Name the parasite shown.
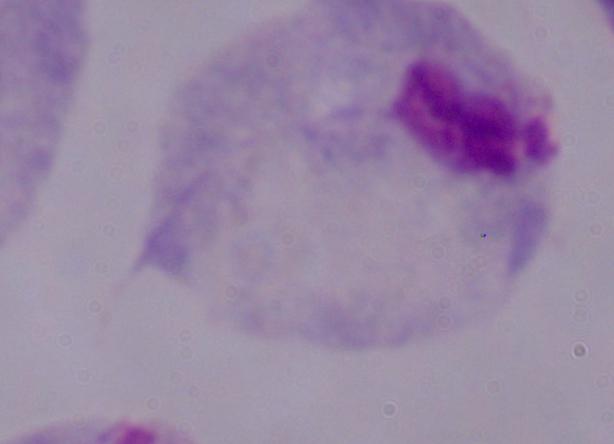
A trichomonad.

magnification = 1000x
modality = micrograph